Assess this cell for malaria.
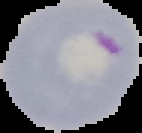
It is parasitized.

{
  "image_size": "142×133 pixels",
  "image_type": "cell region segmented out of the field of view; surrounding area masked to black",
  "preparation": "thin blood film"
}